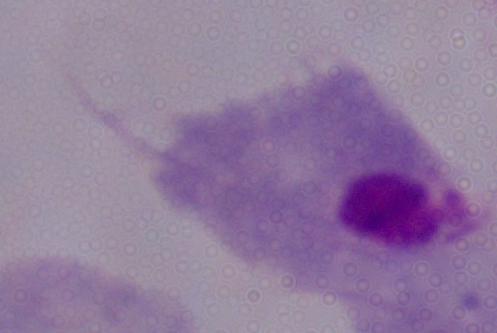
magnification = 1000x
identification = trichomonad
modality = micrograph